Report the malaria status of this cell.
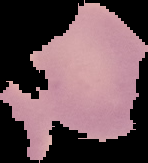
It is uninfected.

{
  "preparation": "thin blood smear",
  "image_type": "segmented cell region with the area outside set to black",
  "image_size": "148×163 pixels"
}